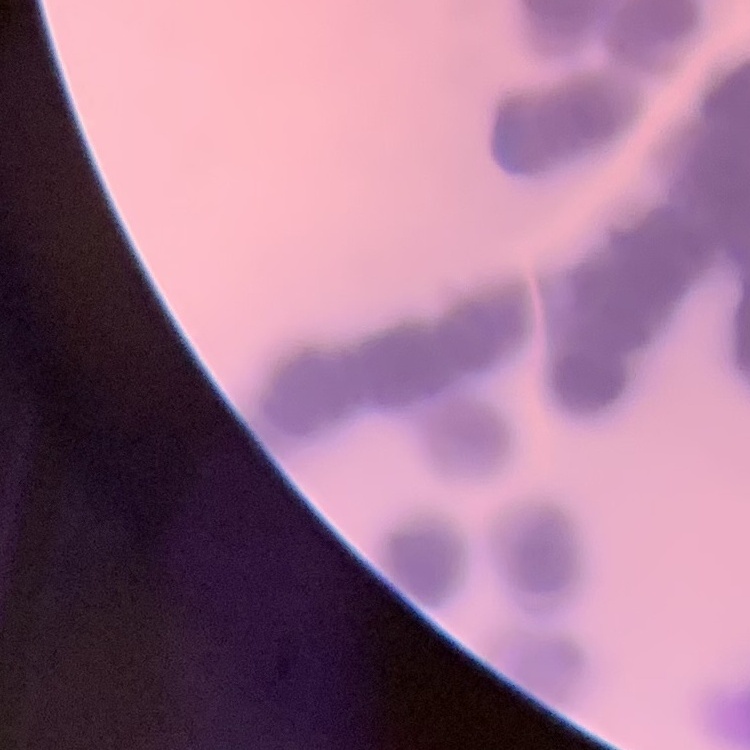

The red blood cells exhibit rouleaux formation. Thin peripheral smear. Square crop of a larger photomicrograph. Stained with either Field's or Giemsa.